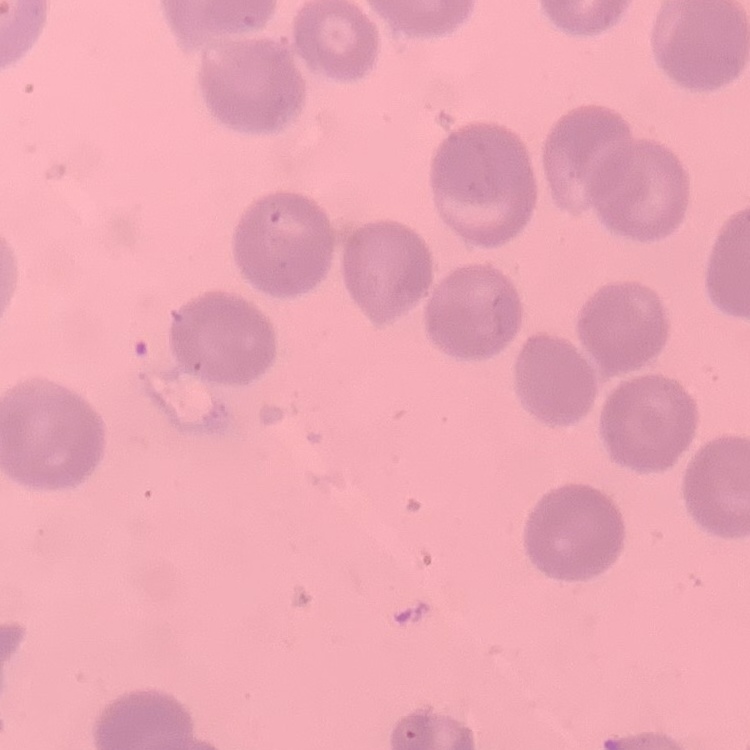

Summary:
  - Red blood cell morphology: no rouleaux formation
  - Image type: one tile cut from a larger photomicrograph
  - Stain: Field's or Giemsa
  - Preparation: thin blood smear